Outline each blood parasite and name the species.
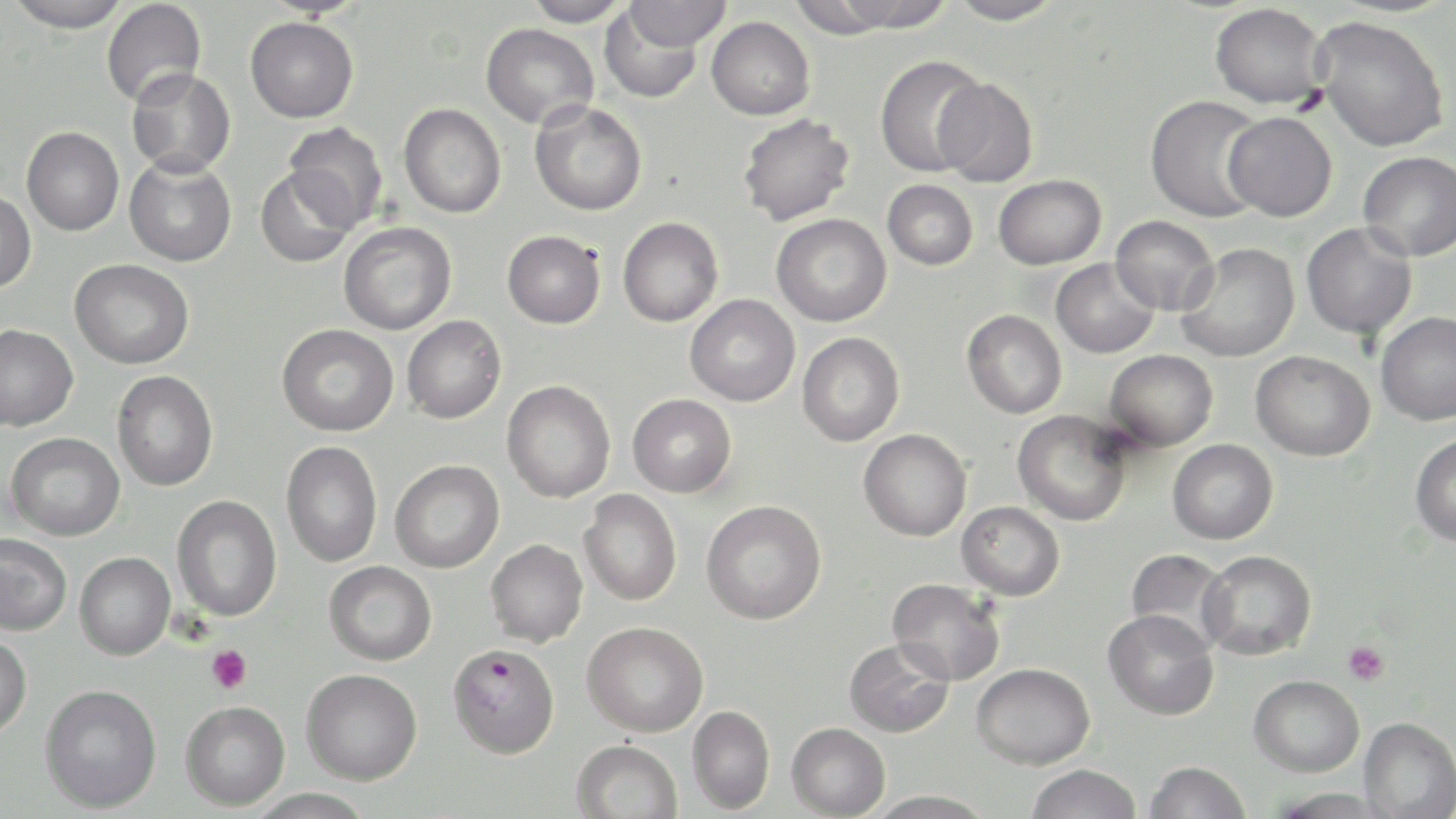
Approximate bounding boxes as (x1,y1)-(x2,y2) corner pairs in pixels.
Plasmodium falciparum-infected red blood cells: (447,643)-(560,759).
No Plasmodium ovale, Plasmodium malariae, Plasmodium vivax, Babesia divergens, or Trypanosoma brucei observed.

slide-level diagnosis = Plasmodium falciparum
preparation = thin blood smear
magnification = 1000x
platelet locations = approximate bounding boxes as (x1,y1)-(x2,y2) corner pairs in pixels: (1343,641)-(1389,685), (206,645)-(252,693)
image size = 1456×819 pixels
modality = light microscopy
uninfected red blood cell locations = approximate bounding boxes as (x1,y1)-(x2,y2) corner pairs in pixels: (5,0)-(132,32), (523,0)-(630,27), (818,0)-(957,32), (946,0)-(1067,25), (101,1)-(206,108), (622,1)-(731,51), (1209,3)-(1329,109), (598,6)-(706,104), (707,16)-(815,120), (1312,16)-(1449,152), (245,17)-(358,123), (481,23)-(598,129), (875,54)-(989,177), (126,68)-(236,177), (934,77)-(1038,187), (1144,94)-(1268,222), (529,101)-(647,216), (398,103)-(506,218), (1222,111)-(1337,221), (737,114)-(855,226), (283,122)-(388,230), (22,127)-(124,236), (1358,151)-(1456,261), (124,156)-(237,266), (256,166)-(357,268), (993,174)-(1106,269), (882,180)-(978,270), (0,191)-(36,293), (771,214)-(892,327), (1110,215)-(1220,317), (617,216)-(723,327), (338,222)-(456,334), (1301,223)-(1417,340), (502,230)-(605,329), (1175,243)-(1299,363), (70,258)-(194,369), (1051,259)-(1159,359), (685,294)-(800,406), (961,309)-(1067,418), (1374,311)-(1456,425), (402,315)-(506,423), (0,324)-(79,431), (277,324)-(398,436), (797,332)-(904,446), (1104,349)-(1218,451), (1250,350)-(1375,461), (112,371)-(218,491), (502,380)-(616,502), (628,394)-(736,497), (1012,410)-(1132,526), (858,429)-(972,541), (5,432)-(125,541), (1409,434)-(1456,546), (1168,439)-(1278,544), (281,441)-(383,567), (390,460)-(504,572), (579,490)-(682,606), (172,495)-(282,621), (701,500)-(826,624), (956,501)-(1065,600), (0,534)-(72,635), (485,539)-(588,646), (1125,548)-(1233,651), (1198,550)-(1316,660), (75,552)-(174,660), (324,561)-(436,665), (887,578)-(1006,686), (1102,609)-(1219,721), (582,621)-(708,736), (0,633)-(32,739), (844,637)-(954,737), (971,662)-(1095,769), (301,668)-(422,785), (1248,674)-(1364,776), (39,683)-(162,813), (180,700)-(290,811), (686,705)-(775,813), (1358,716)-(1456,818), (786,722)-(890,818), (570,739)-(683,819), (1144,761)-(1251,819), (1026,763)-(1142,819), (246,788)-(376,818), (867,790)-(996,818)
stain = May-Grünwald-Giemsa
field of view = one of a larger specimen